Comment on the morphology of the red blood cells.
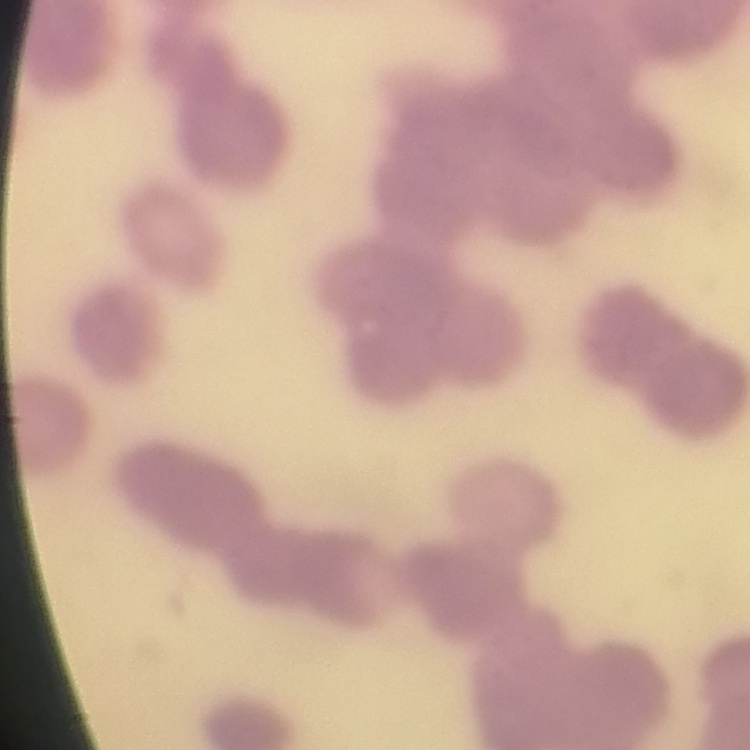
Rouleaux formation.

Summary:
  - Preparation: thin blood smear
  - Stain: Field's or Giemsa
  - Image type: one tile cut from a larger photomicrograph